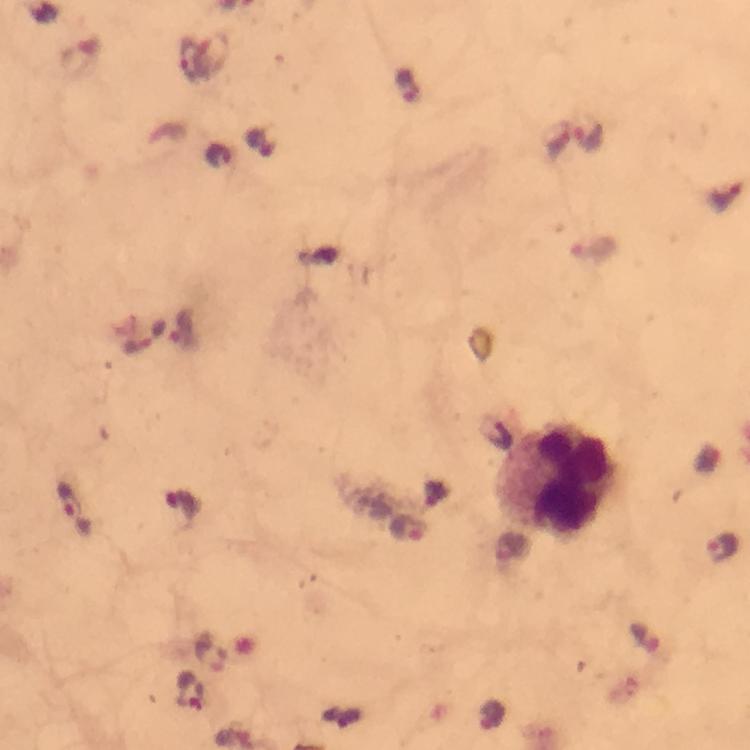

Approximate centers as [x, y] in pixels. Leukocyte locations: [563, 482]. Plasmodium parasite locations: [189, 60], [407, 85], [588, 134], [558, 140], [724, 197], [183, 329], [144, 338], [494, 432], [181, 504], [73, 508], [408, 530], [722, 547], [190, 689], [493, 717]. 100x magnification. Giemsa stain. Thick blood smear. Photographed with a smartphone mounted on the microscope. Immersion oil applied. From a malaria diagnostic workup. A crop from one field of view. Image is 750×750 pixels.